Describe the morphology of the red blood cells.
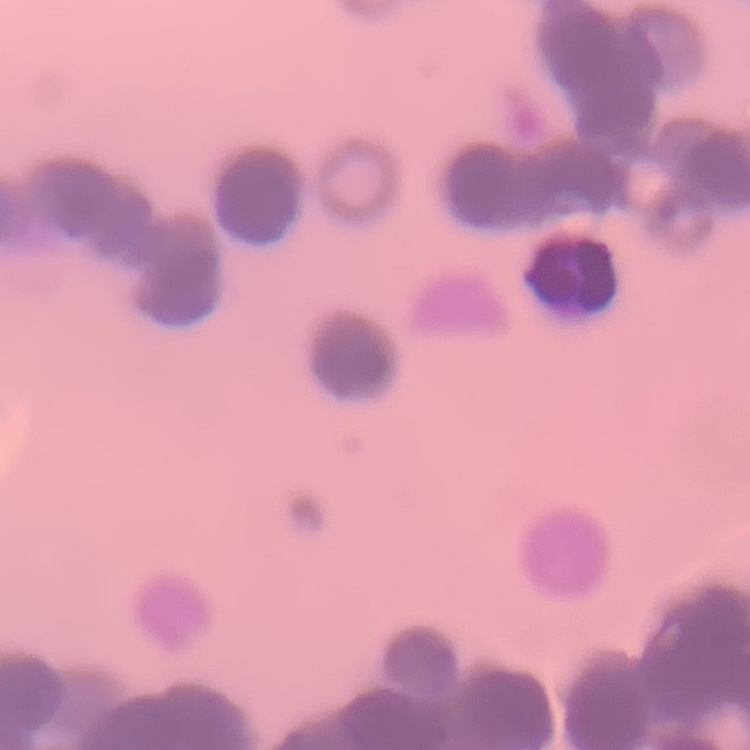

Rouleaux formation.

image type = one tile cut from a larger photomicrograph
preparation = thin blood film
stain = Field's or Giemsa